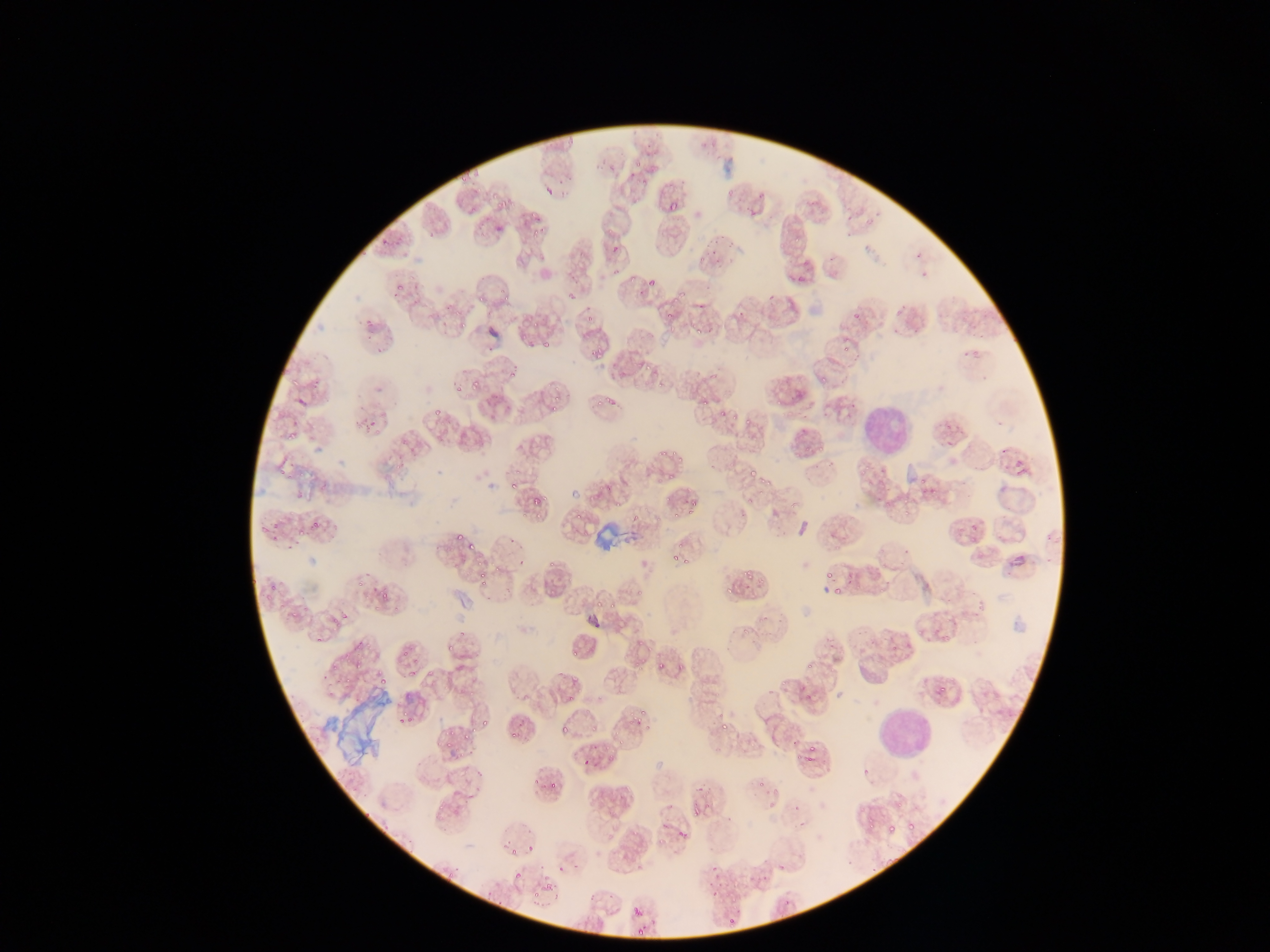

Approximate bounding boxes as [left, top, right, bottom] in pixels.
Summary:
  - Plasmodium parasite locations: [724, 178, 742, 194], [754, 193, 770, 201], [494, 196, 512, 211], [467, 203, 476, 215], [665, 205, 676, 217], [528, 227, 539, 241], [377, 233, 391, 250], [709, 237, 731, 256], [611, 241, 628, 254], [708, 258, 725, 267], [918, 260, 932, 279], [609, 263, 621, 278], [793, 267, 814, 283], [645, 273, 662, 295], [391, 278, 408, 293], [765, 285, 776, 299], [500, 286, 509, 299], [565, 289, 578, 301], [479, 291, 494, 306], [670, 292, 689, 301], [739, 301, 752, 318], [452, 304, 462, 314], [662, 308, 672, 321], [852, 308, 866, 317], [588, 312, 597, 321], [689, 316, 710, 335], [459, 317, 468, 329], [365, 318, 379, 336], [532, 318, 546, 327], [535, 332, 557, 351], [587, 340, 606, 359], [839, 342, 855, 357], [962, 345, 977, 363], [636, 363, 643, 371], [504, 365, 514, 382], [656, 368, 675, 388], [821, 376, 834, 385], [469, 377, 480, 392], [449, 378, 462, 395], [599, 381, 626, 411], [772, 390, 789, 407], [697, 391, 714, 403], [548, 396, 563, 413], [289, 400, 304, 414], [716, 400, 729, 417], [426, 401, 445, 418], [725, 404, 737, 423], [362, 412, 383, 430], [746, 420, 753, 428], [282, 431, 293, 448], [947, 437, 956, 448], [999, 441, 1009, 457], [814, 442, 828, 451], [656, 445, 673, 459], [285, 454, 306, 480], [827, 456, 844, 471], [1014, 456, 1035, 475], [748, 457, 763, 472], [664, 469, 679, 477], [509, 472, 520, 484], [756, 474, 768, 484], [918, 475, 933, 490], [509, 481, 518, 498], [533, 494, 546, 505], [744, 494, 758, 504], [689, 496, 703, 515], [899, 500, 914, 519], [768, 505, 781, 520], [670, 509, 680, 522], [307, 515, 326, 536], [572, 515, 591, 524], [967, 519, 983, 533], [291, 521, 304, 543], [265, 522, 276, 539], [454, 527, 467, 542], [468, 541, 475, 551], [897, 541, 914, 555], [1008, 544, 1029, 572], [667, 546, 684, 561], [545, 555, 560, 570], [687, 557, 692, 572], [742, 566, 751, 578], [478, 568, 489, 583], [821, 570, 843, 580], [831, 576, 845, 596], [725, 578, 744, 592], [376, 590, 388, 602], [588, 601, 605, 612], [607, 601, 622, 609], [282, 610, 291, 618], [912, 622, 927, 637], [938, 624, 957, 639], [305, 633, 322, 645], [636, 634, 649, 650], [569, 640, 582, 662], [397, 648, 418, 662], [351, 656, 369, 671], [656, 657, 665, 670], [802, 657, 823, 674], [325, 659, 338, 674], [629, 659, 647, 677], [778, 667, 793, 691], [404, 670, 415, 683], [341, 675, 352, 691], [374, 677, 387, 690], [936, 680, 951, 694], [563, 690, 576, 701], [631, 694, 650, 722], [397, 706, 418, 725], [480, 706, 504, 726], [714, 713, 736, 735], [556, 718, 578, 738], [505, 724, 519, 741], [591, 726, 601, 733], [437, 730, 458, 750], [459, 731, 471, 745], [580, 745, 599, 767], [803, 745, 817, 758], [858, 767, 869, 778], [549, 771, 565, 790], [758, 775, 769, 793], [439, 791, 456, 814], [693, 792, 719, 815], [790, 805, 798, 814], [864, 814, 879, 831], [794, 815, 805, 829], [902, 817, 920, 837], [885, 819, 895, 833], [674, 822, 698, 850], [524, 843, 539, 856], [505, 847, 519, 858], [780, 857, 790, 870], [706, 860, 718, 873], [867, 862, 879, 872], [511, 863, 525, 882], [543, 866, 557, 885], [761, 871, 766, 883], [525, 884, 544, 899], [709, 891, 726, 900], [784, 899, 794, 909], [631, 906, 644, 920], [727, 909, 738, 926], [633, 926, 649, 941]
  - Leukocyte locations: [860, 396, 916, 463], [871, 704, 935, 765]
  - Country: Ghana
  - Image size: 1270×952 pixels
  - Capture: mobile-phone photograph through a microscope
  - Preparation: thin blood smear
  - Field of view: single